State which parasite is depicted.
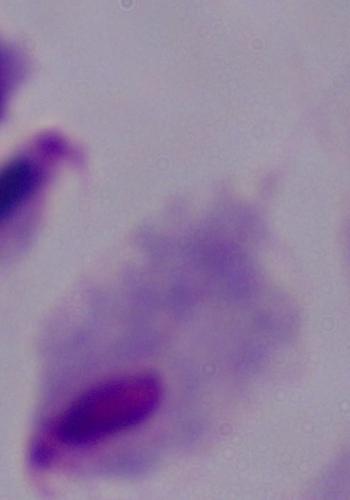
This is a trichomonad.

modality = photomicrograph
magnification = 1000x